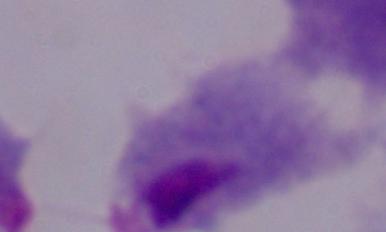

Summary:
  - Identification: trichomonad
  - Modality: micrograph
  - Magnification: 1000x